Point out each Plasmodium parasite and each leukocyte.
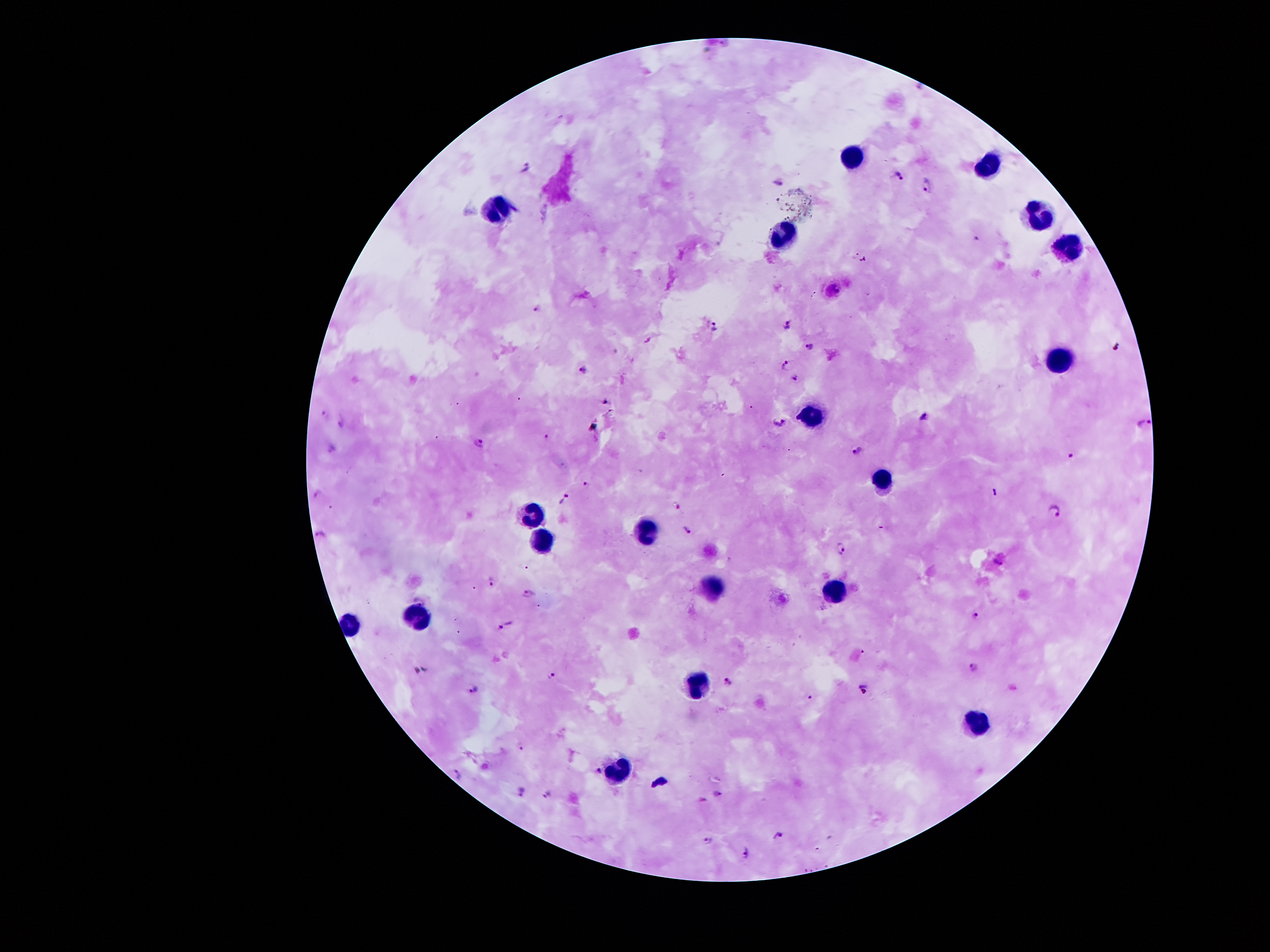

Approximate centers as [x, y] in pixels.
Plasmodium parasites: [527, 165], [897, 175], [780, 184], [926, 184], [978, 236], [537, 307], [714, 326], [787, 326], [811, 345], [1120, 346], [786, 363], [585, 369], [795, 377], [325, 413], [923, 415], [1145, 421], [340, 422], [780, 423], [548, 436], [478, 442], [332, 449], [857, 449], [1071, 459], [588, 484], [994, 493], [317, 494], [564, 499], [678, 506], [1054, 512], [687, 529], [323, 532], [843, 548], [998, 562], [490, 582], [527, 592], [974, 615], [506, 625], [975, 666], [552, 675], [728, 681], [473, 689], [864, 689], [519, 747], [598, 771], [458, 776], [521, 791], [715, 793], [547, 794], [701, 799], [778, 835], [707, 838], [745, 853].
Leukocytes: [853, 157], [988, 164], [497, 207], [1037, 214], [785, 237], [1069, 247], [1060, 359], [816, 415], [880, 477], [529, 513], [643, 529], [539, 538], [710, 587], [834, 591], [414, 614], [346, 624], [696, 684], [976, 722], [618, 775].

Single field of view. Patient malaria status: positive for Plasmodium falciparum. Image is 1270×952 pixels. 100x magnification. Giemsa-stained preparation. Smartphone photograph taken through the microscope eyepiece. Thick blood film.